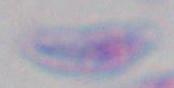
magnification = 1000x
modality = photomicrograph
identification = Toxoplasma gondii